State which parasite is depicted.
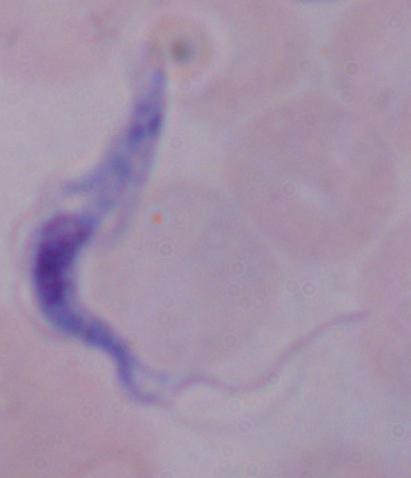
This is a trypanosome.

modality = photomicrograph
magnification = 1000x